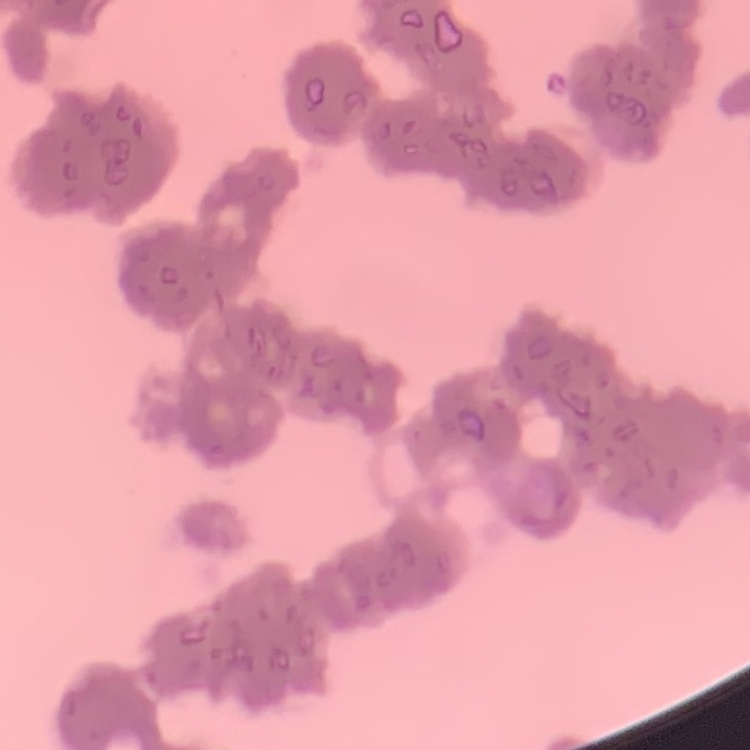
Summary:
  - Red blood cell morphology: rouleaux formation
  - Preparation: thin peripheral smear
  - Image type: square crop of a larger photomicrograph
  - Stain: Field's or Giemsa